Point out each Plasmodium parasite.
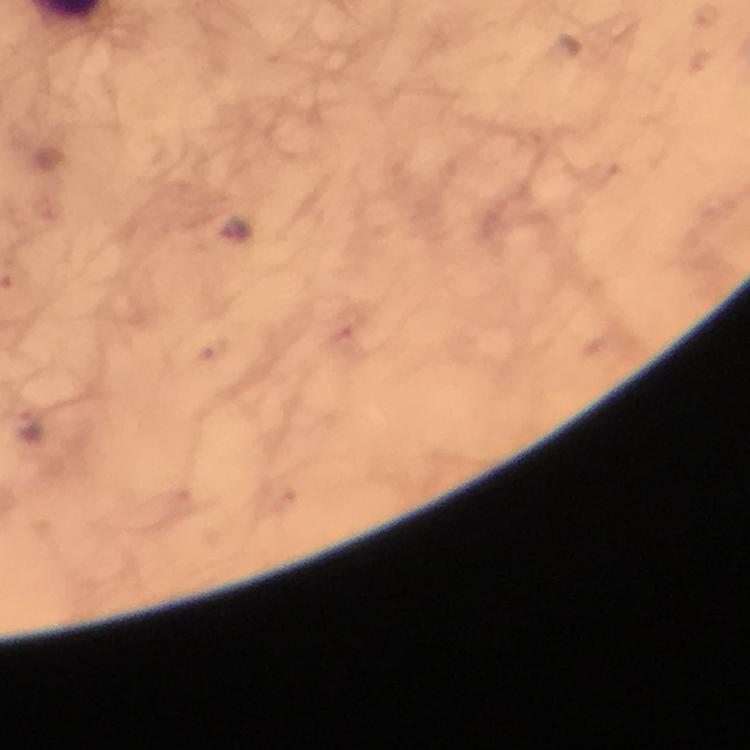
Approximate centers as {x, y} in pixels.
Plasmodium parasites: {235, 235}, {28, 423}.

Summary:
  - Image size: 750×750 pixels
  - Stain: Giemsa
  - Context: from a malaria diagnostic workup
  - Magnification: 100x
  - Preparation: thick smear
  - Cropped from: one field of view
  - Immersion oil: applied
  - Capture: smartphone mounted on the microscope